Outline each blood parasite and name the species.
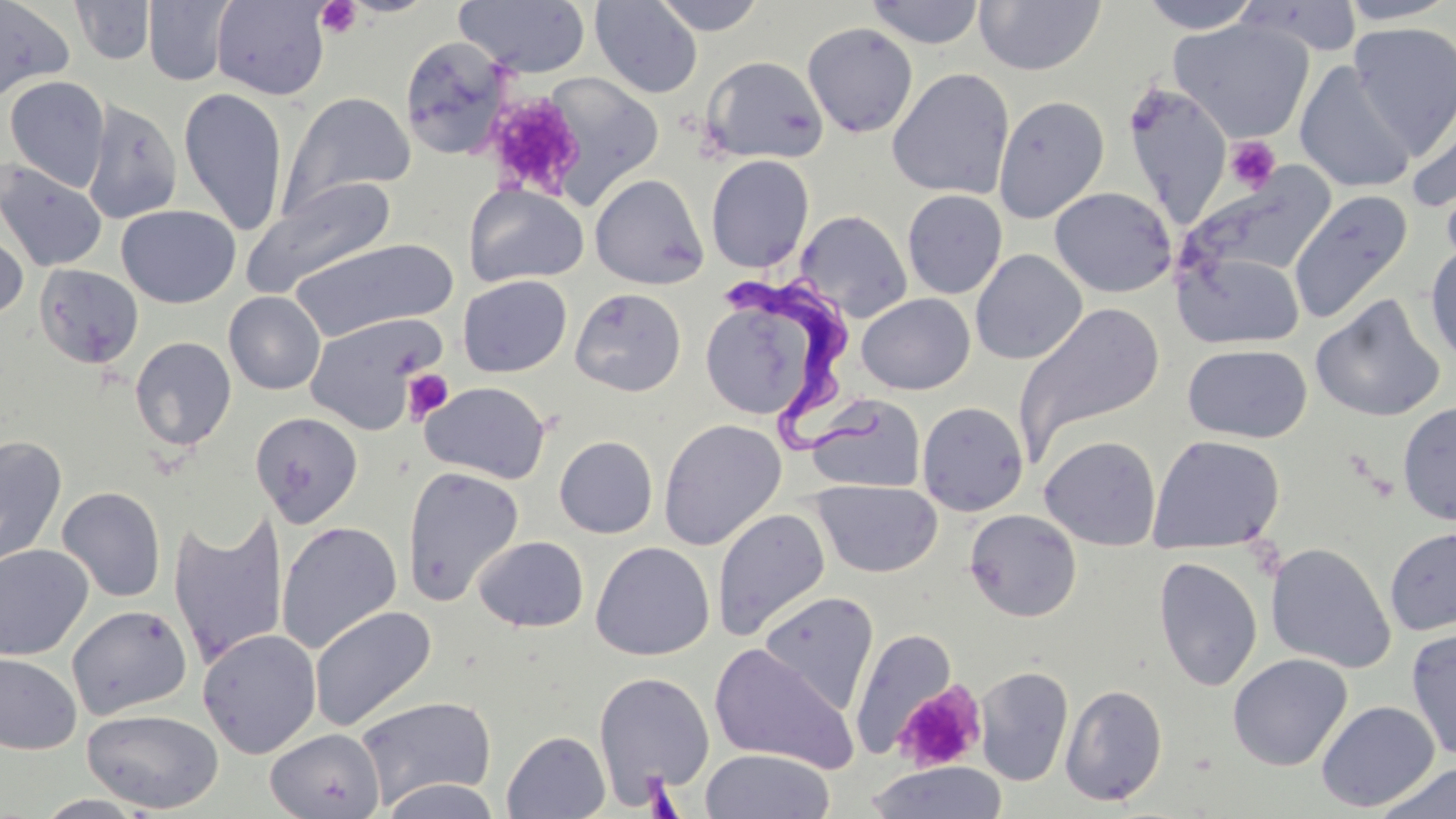
Approximate bounding boxes as named x1/y1/x2/y2 corners in pixels.
Trypanosoma brucei: (x1=724, y1=270, x2=893, y2=454).
No Plasmodium falciparum, Plasmodium ovale, Plasmodium malariae, Plasmodium vivax, or Babesia divergens observed.

slide-level diagnosis = Trypanosoma brucei
modality = optical microscopy
stain = May-Grünwald-Giemsa
field of view = single
preparation = thin blood film
image size = 1456×819 pixels
uninfected red blood cell locations = approximate bounding boxes as named x1/y1/x2/y2 corners in pixels: (x1=143, y1=0, x2=235, y2=86), (x1=652, y1=0, x2=768, y2=36), (x1=865, y1=0, x2=985, y2=49), (x1=1136, y1=0, x2=1264, y2=33), (x1=0, y1=1, x2=74, y2=101), (x1=70, y1=1, x2=156, y2=65), (x1=210, y1=1, x2=331, y2=100), (x1=455, y1=1, x2=591, y2=77), (x1=590, y1=1, x2=703, y2=98), (x1=973, y1=1, x2=1106, y2=76), (x1=1336, y1=1, x2=1455, y2=25), (x1=1170, y1=18, x2=1315, y2=143), (x1=1348, y1=21, x2=1456, y2=154), (x1=802, y1=22, x2=918, y2=138), (x1=398, y1=35, x2=514, y2=160), (x1=700, y1=55, x2=829, y2=165), (x1=1295, y1=62, x2=1417, y2=194), (x1=887, y1=68, x2=1015, y2=199), (x1=534, y1=72, x2=666, y2=208), (x1=4, y1=76, x2=110, y2=192), (x1=1124, y1=85, x2=1233, y2=224), (x1=178, y1=87, x2=289, y2=235), (x1=1406, y1=91, x2=1456, y2=218), (x1=280, y1=92, x2=415, y2=215), (x1=993, y1=95, x2=1110, y2=223), (x1=82, y1=98, x2=183, y2=224), (x1=705, y1=154, x2=815, y2=273), (x1=0, y1=160, x2=108, y2=272), (x1=1183, y1=166, x2=1336, y2=287), (x1=589, y1=174, x2=709, y2=290), (x1=243, y1=177, x2=397, y2=297), (x1=464, y1=183, x2=588, y2=288), (x1=1049, y1=186, x2=1176, y2=297), (x1=1287, y1=189, x2=1414, y2=325), (x1=902, y1=190, x2=1007, y2=299), (x1=116, y1=205, x2=240, y2=309), (x1=796, y1=209, x2=912, y2=323), (x1=0, y1=223, x2=28, y2=325), (x1=289, y1=238, x2=457, y2=342), (x1=1424, y1=241, x2=1456, y2=366), (x1=1175, y1=248, x2=1305, y2=350), (x1=970, y1=249, x2=1087, y2=365), (x1=34, y1=264, x2=144, y2=369), (x1=458, y1=275, x2=573, y2=377), (x1=698, y1=284, x2=840, y2=426), (x1=570, y1=287, x2=687, y2=397), (x1=224, y1=291, x2=325, y2=394), (x1=856, y1=293, x2=975, y2=395), (x1=1310, y1=295, x2=1446, y2=422), (x1=1014, y1=301, x2=1166, y2=456), (x1=303, y1=312, x2=447, y2=434), (x1=130, y1=336, x2=237, y2=451), (x1=1182, y1=344, x2=1312, y2=443), (x1=420, y1=380, x2=551, y2=484), (x1=807, y1=394, x2=926, y2=493), (x1=917, y1=401, x2=1029, y2=516), (x1=1397, y1=401, x2=1456, y2=525), (x1=250, y1=412, x2=364, y2=527), (x1=658, y1=418, x2=787, y2=550), (x1=1148, y1=434, x2=1285, y2=555), (x1=0, y1=435, x2=67, y2=568), (x1=554, y1=435, x2=658, y2=538), (x1=1039, y1=436, x2=1162, y2=550), (x1=401, y1=465, x2=525, y2=606), (x1=810, y1=480, x2=942, y2=578), (x1=57, y1=486, x2=166, y2=603), (x1=712, y1=507, x2=831, y2=641), (x1=965, y1=509, x2=1082, y2=622), (x1=168, y1=511, x2=289, y2=666), (x1=276, y1=521, x2=402, y2=654), (x1=1384, y1=526, x2=1456, y2=636), (x1=474, y1=535, x2=588, y2=633), (x1=591, y1=541, x2=715, y2=661), (x1=1265, y1=542, x2=1396, y2=673), (x1=0, y1=544, x2=94, y2=661), (x1=1153, y1=556, x2=1263, y2=691), (x1=758, y1=591, x2=880, y2=713), (x1=67, y1=604, x2=193, y2=720), (x1=309, y1=605, x2=437, y2=732), (x1=197, y1=628, x2=322, y2=759), (x1=850, y1=628, x2=959, y2=757), (x1=1406, y1=628, x2=1456, y2=761), (x1=708, y1=643, x2=859, y2=773), (x1=0, y1=653, x2=81, y2=755), (x1=1228, y1=653, x2=1352, y2=771), (x1=974, y1=666, x2=1074, y2=787), (x1=593, y1=672, x2=714, y2=799), (x1=1060, y1=683, x2=1168, y2=806), (x1=355, y1=694, x2=496, y2=809), (x1=1316, y1=700, x2=1440, y2=812), (x1=81, y1=707, x2=224, y2=814), (x1=265, y1=728, x2=384, y2=819), (x1=502, y1=730, x2=610, y2=818), (x1=699, y1=749, x2=835, y2=819), (x1=865, y1=761, x2=1008, y2=819), (x1=1375, y1=763, x2=1455, y2=819), (x1=380, y1=778, x2=502, y2=819)
magnification = 1000x
platelet locations = approximate bounding boxes as named x1/y1/x2/y2 corners in pixels: (x1=315, y1=1, x2=362, y2=38), (x1=483, y1=91, x2=585, y2=200), (x1=1224, y1=136, x2=1281, y2=193), (x1=402, y1=369, x2=454, y2=423), (x1=892, y1=680, x2=987, y2=774)